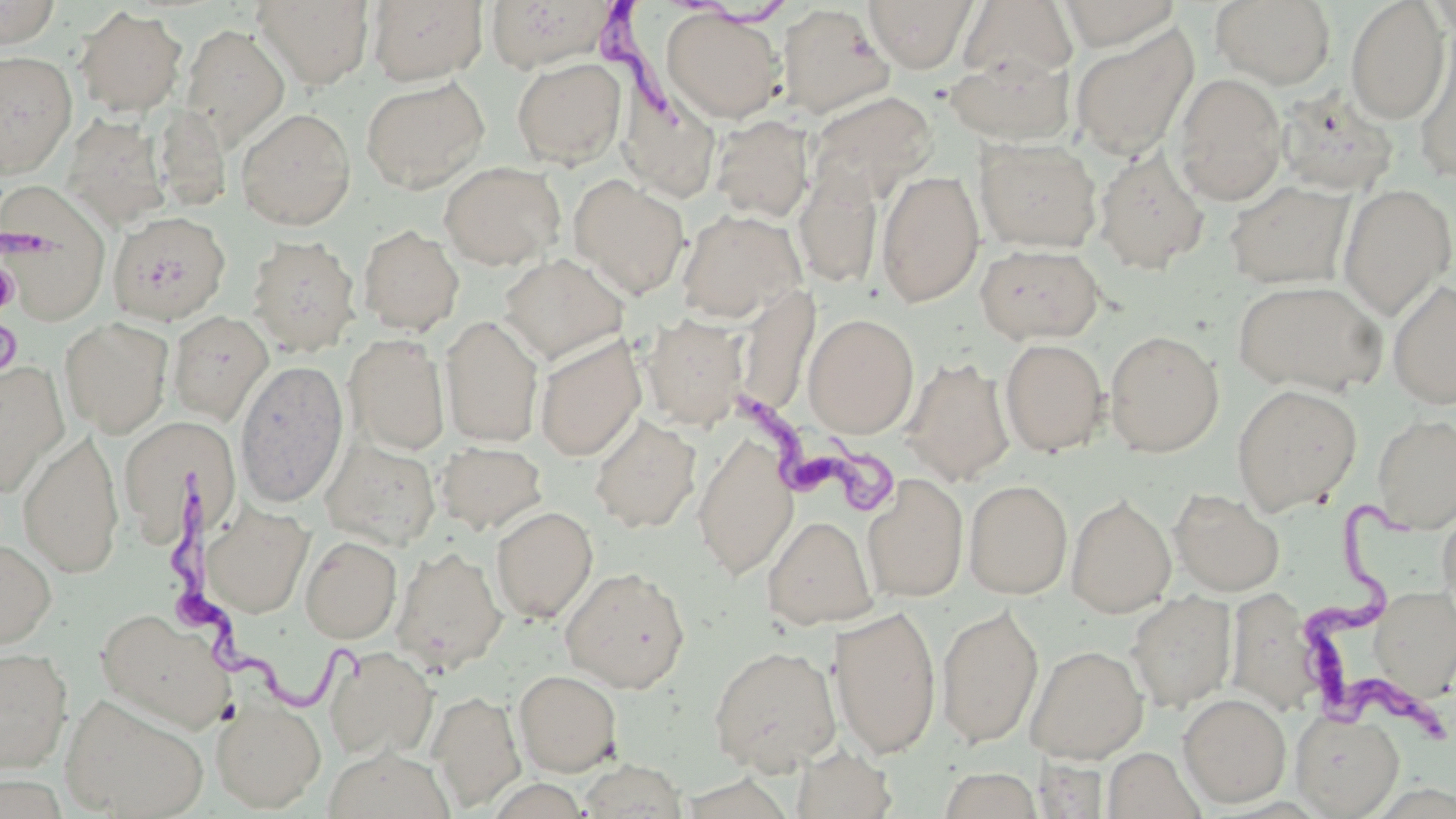

Summary:
  - Coordinate format: approximate bounding boxes as [x1, y1, x2, y2] in pixels
  - Uninfected red blood cell locations: [252, 0, 375, 89], [367, 0, 487, 85], [484, 0, 619, 72], [863, 0, 977, 72], [1056, 0, 1182, 50], [0, 1, 61, 49], [958, 1, 1078, 86], [1210, 1, 1336, 88], [1345, 1, 1450, 123], [777, 4, 895, 120], [73, 6, 187, 117], [660, 8, 786, 124], [181, 24, 290, 149], [1069, 24, 1200, 161], [1412, 35, 1456, 184], [0, 50, 77, 179], [944, 51, 1075, 146], [511, 57, 627, 168], [1172, 73, 1287, 206], [360, 76, 490, 194], [618, 84, 722, 202], [1275, 86, 1400, 197], [806, 91, 936, 207], [153, 106, 231, 211], [236, 107, 357, 231], [62, 113, 170, 228], [709, 114, 814, 223], [974, 136, 1103, 253], [1093, 147, 1210, 274], [439, 161, 566, 271], [794, 167, 884, 289], [876, 169, 985, 307], [569, 175, 690, 300], [0, 179, 112, 325], [1225, 179, 1354, 290], [1337, 183, 1455, 320], [676, 208, 806, 323], [111, 218, 239, 333], [358, 224, 464, 336], [247, 234, 360, 356], [975, 243, 1105, 344], [498, 253, 628, 365], [1232, 279, 1387, 396], [1388, 279, 1456, 410], [168, 310, 273, 424], [642, 313, 747, 429], [803, 313, 919, 437], [440, 314, 544, 448], [60, 317, 173, 437], [1105, 329, 1224, 457], [344, 334, 451, 455], [535, 335, 646, 461], [999, 338, 1108, 456], [901, 357, 1016, 486], [235, 359, 349, 508], [0, 361, 68, 496], [1230, 384, 1362, 515], [589, 413, 701, 534], [1373, 413, 1456, 532], [119, 416, 241, 541], [18, 428, 124, 579], [693, 433, 799, 580], [320, 437, 441, 549], [436, 441, 547, 534], [862, 473, 969, 602], [964, 479, 1073, 599], [1170, 489, 1285, 597], [1066, 495, 1177, 618], [203, 504, 315, 618], [1438, 505, 1456, 614], [491, 506, 598, 623], [762, 514, 877, 630], [300, 535, 402, 643], [0, 537, 57, 650], [391, 544, 507, 674], [560, 567, 691, 692], [1370, 585, 1456, 699], [1226, 587, 1323, 716], [1127, 591, 1237, 711], [936, 603, 1044, 747], [829, 604, 942, 759], [95, 607, 236, 732], [708, 644, 841, 773], [1026, 644, 1148, 763], [324, 646, 438, 760], [0, 647, 74, 773], [514, 669, 622, 776], [428, 689, 526, 811], [60, 693, 209, 818], [1178, 693, 1291, 807], [210, 696, 326, 812], [1291, 710, 1404, 817], [791, 745, 897, 819], [1102, 746, 1205, 819], [322, 747, 455, 819], [1034, 757, 1110, 818], [576, 760, 690, 818], [938, 767, 1043, 819]
  - Trypanosoma brucei locations: [593, 0, 788, 124], [0, 225, 62, 368], [733, 391, 904, 515], [166, 470, 373, 706], [1294, 493, 1455, 737]
  - Slide-level diagnosis: Trypanosoma brucei
  - Preparation: thin blood film
  - Field of view: one of a larger specimen
  - Image size: 1456×819 pixels
  - Stain: May-Grünwald-Giemsa
  - Modality: optical microscopy
  - Magnification: 1000x